Identify the cell.
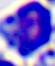

This is a leukocyte.

400x magnification. Micrograph.